Classify this cell by malaria status.
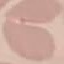
Uninfected.

Summary:
  - Stain: Giemsa
  - Capture: smartphone camera at the microscope eyepiece
  - Image type: cell patch, automatically extracted from a larger field of view and resized to 64 × 64 pixels
  - Preparation: thin smear